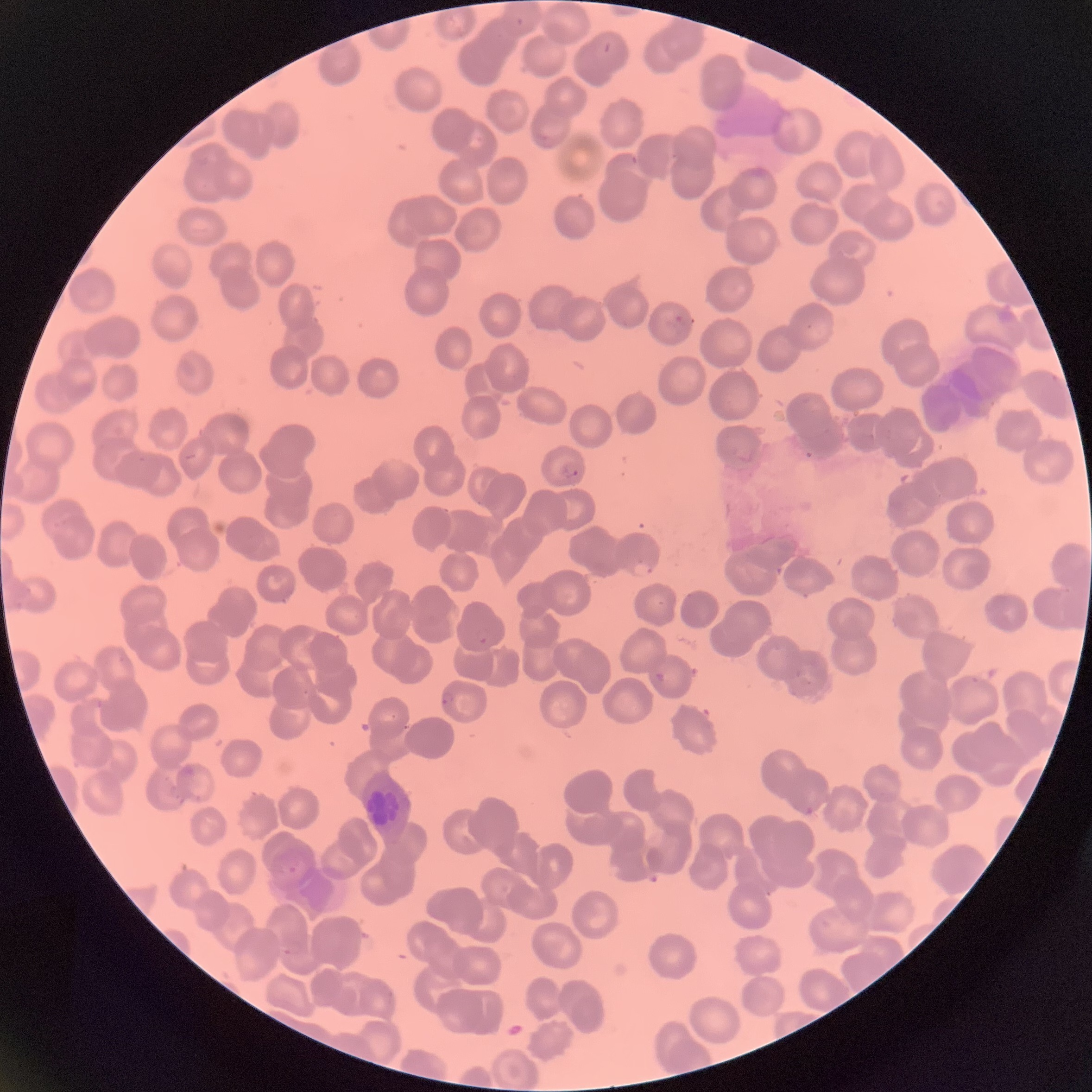 Approximate bounding boxes as (x1, y1, x2, y2) in pixels. Plasmodium parasite locations: (516, 16, 524, 25), (537, 133, 547, 143), (629, 155, 640, 165), (668, 308, 683, 325), (561, 465, 580, 480), (635, 561, 655, 577), (474, 628, 491, 645), (440, 690, 456, 705), (380, 709, 397, 722), (282, 937, 304, 958). Optical microscopy. Image is 1092×1092 pixels. Thin blood smear. The red blood cells show rouleaux formation.